Give the position of every Plasmodium parasite visible.
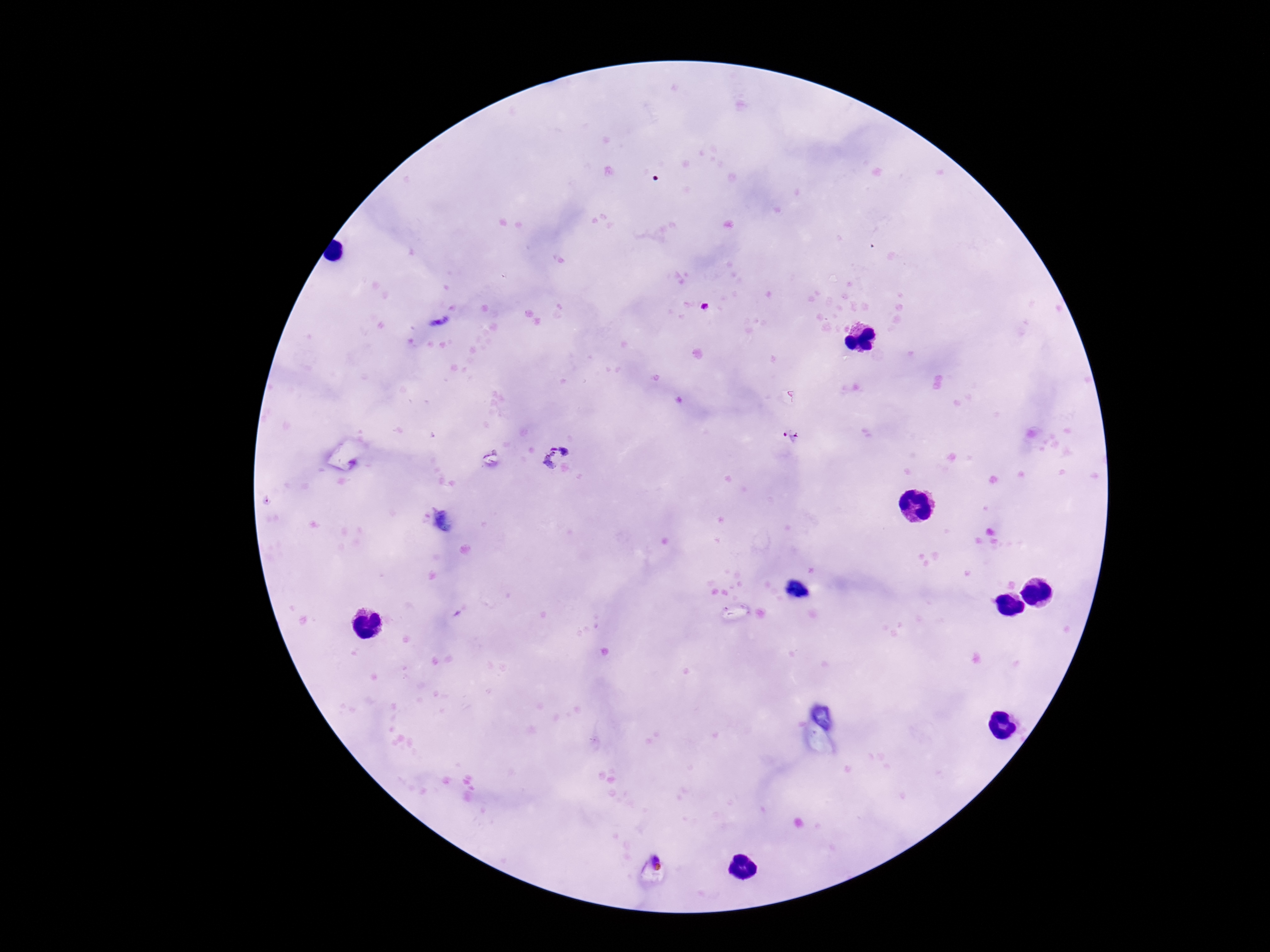
Approximate centers as (x, y) in pixels.
Plasmodium parasites: (707, 308), (791, 436).

Smartphone photograph taken through the microscope eyepiece. Patient malaria status: infected. Giemsa-stained preparation. 100x magnification. Image is 1270×952 pixels. Thick blood film. One field from this slide.